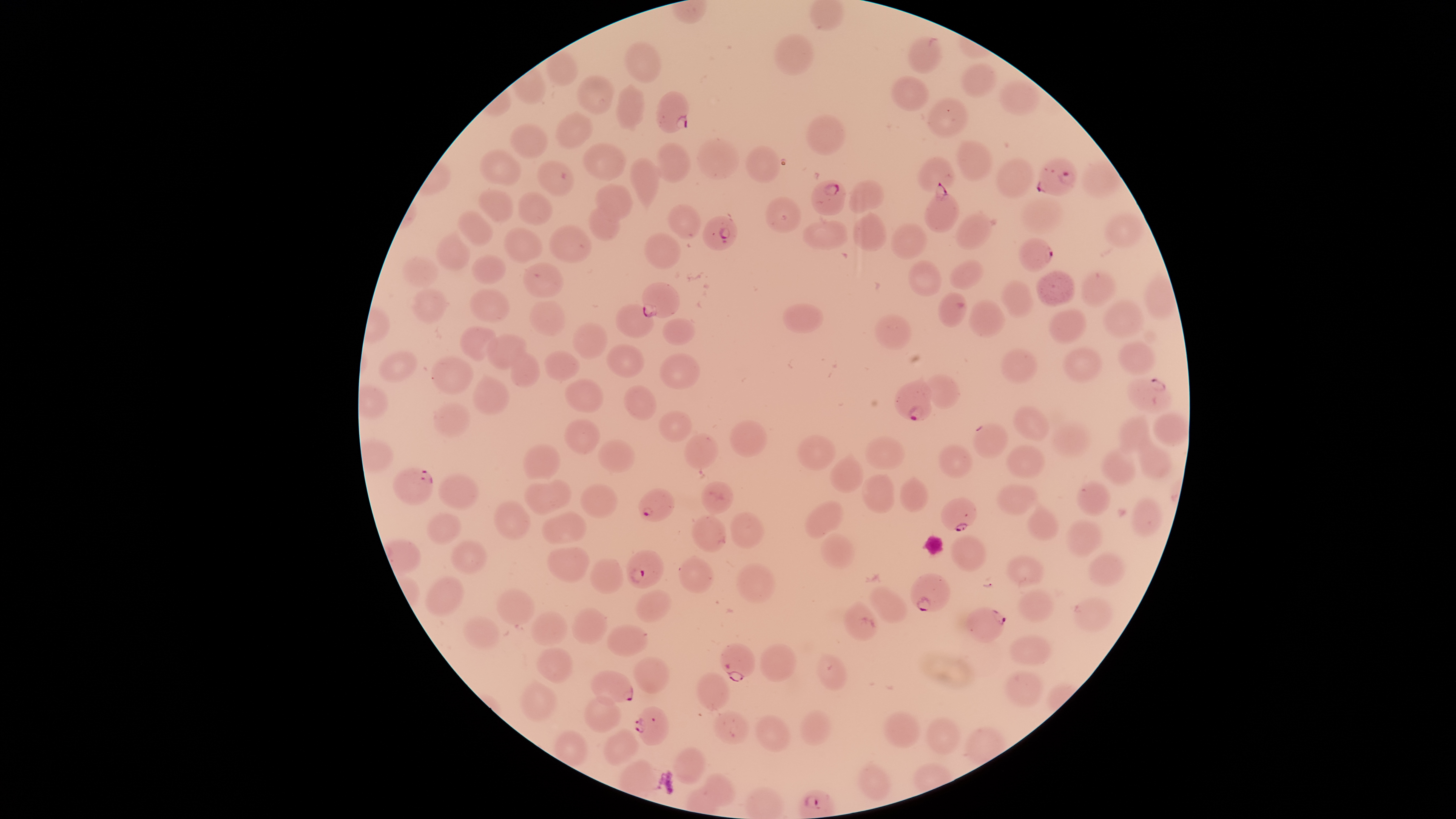
Approximate bounding boxes as [left, top, right, bottom] in pixels.
Summary:
  - Parasitized RBCs: [655, 90, 690, 134], [1036, 156, 1078, 196], [810, 180, 847, 216], [923, 182, 960, 232], [701, 214, 738, 251], [1017, 236, 1054, 273], [642, 282, 680, 318], [894, 374, 933, 421], [1125, 376, 1172, 413], [392, 466, 435, 506], [637, 486, 675, 522], [940, 497, 978, 532], [626, 549, 665, 589], [910, 572, 951, 613], [964, 607, 1007, 643], [719, 642, 756, 682], [590, 670, 633, 706], [633, 705, 670, 746]
  - Uninfected RBCs: [773, 33, 816, 75], [907, 34, 941, 73], [624, 39, 662, 84], [546, 50, 579, 87], [960, 63, 997, 97], [576, 73, 615, 115], [890, 75, 930, 111], [999, 78, 1040, 116], [616, 82, 646, 132], [926, 97, 969, 137], [555, 111, 594, 150], [806, 113, 847, 156], [509, 122, 550, 159], [696, 137, 740, 181], [954, 139, 993, 182], [581, 141, 627, 181], [653, 142, 692, 184], [745, 144, 780, 184], [479, 148, 522, 185], [995, 155, 1036, 198], [628, 156, 663, 213], [917, 156, 955, 191], [537, 159, 575, 197], [1081, 159, 1122, 199], [848, 179, 884, 214], [594, 183, 633, 222], [476, 188, 514, 223], [518, 190, 554, 226], [765, 195, 801, 234], [1021, 197, 1063, 232], [668, 204, 702, 240], [589, 207, 620, 242], [456, 209, 494, 247], [852, 211, 888, 252], [955, 211, 995, 249], [1103, 212, 1147, 249], [802, 220, 849, 249], [890, 222, 929, 260], [548, 223, 593, 264], [503, 226, 544, 264], [434, 228, 471, 271], [643, 232, 681, 271], [471, 254, 507, 285], [402, 256, 438, 288], [948, 259, 985, 291], [907, 260, 942, 296], [522, 261, 564, 298], [1035, 269, 1076, 307], [1081, 269, 1118, 307], [1000, 278, 1035, 319], [410, 286, 450, 325], [468, 288, 510, 322], [937, 292, 968, 328], [968, 298, 1006, 338], [1101, 298, 1146, 340], [528, 300, 567, 336], [615, 303, 655, 339], [781, 303, 824, 334], [1048, 307, 1087, 345], [874, 313, 912, 350], [662, 317, 697, 345], [572, 321, 609, 359], [459, 325, 497, 361], [486, 333, 528, 370], [1117, 340, 1156, 376], [605, 344, 645, 378], [1000, 347, 1039, 384], [1063, 347, 1104, 383], [377, 350, 417, 384], [509, 350, 541, 388], [543, 350, 581, 382], [659, 352, 700, 390], [430, 355, 475, 395], [921, 373, 961, 409], [472, 374, 510, 416], [564, 379, 604, 413], [624, 385, 658, 421], [433, 400, 471, 438], [1011, 405, 1051, 442], [657, 410, 692, 443], [1152, 413, 1188, 446], [1116, 414, 1150, 455], [563, 418, 601, 455], [729, 419, 769, 457], [972, 422, 1008, 459], [1050, 422, 1091, 458], [683, 431, 720, 471], [1137, 431, 1173, 481], [796, 434, 836, 471], [864, 434, 905, 470], [597, 439, 635, 473], [522, 443, 560, 479], [936, 444, 973, 478], [1005, 445, 1047, 480], [1099, 446, 1136, 486], [829, 450, 864, 493], [860, 472, 895, 514], [438, 473, 480, 512], [899, 475, 929, 513], [547, 479, 572, 508], [1074, 479, 1112, 516], [701, 480, 735, 515], [524, 483, 556, 516], [580, 483, 618, 519], [995, 484, 1038, 516], [1026, 497, 1060, 541], [1130, 497, 1162, 537], [803, 499, 844, 540], [493, 501, 532, 540], [541, 511, 588, 545], [729, 511, 765, 548], [426, 512, 462, 546], [691, 513, 726, 553], [1065, 518, 1105, 558], [820, 532, 856, 569], [949, 534, 987, 572], [449, 540, 488, 575], [546, 546, 590, 583], [1087, 552, 1126, 587], [1004, 553, 1046, 587], [678, 554, 715, 594], [589, 558, 624, 594], [735, 562, 776, 603], [424, 575, 465, 616], [869, 584, 909, 623], [495, 586, 535, 626], [1016, 588, 1055, 623], [636, 589, 673, 623], [1071, 596, 1114, 632], [842, 599, 881, 641], [571, 607, 608, 645], [531, 610, 568, 647], [462, 615, 500, 649], [606, 624, 648, 658], [1009, 634, 1054, 666], [759, 642, 797, 683], [535, 647, 573, 684], [816, 652, 847, 690], [632, 656, 670, 695], [1003, 670, 1045, 708], [696, 671, 730, 711], [519, 678, 558, 721], [584, 693, 622, 733], [799, 709, 832, 747], [713, 710, 750, 744], [882, 711, 922, 749], [754, 714, 791, 752], [925, 716, 962, 755], [602, 728, 640, 766], [552, 729, 589, 767], [672, 746, 706, 785], [855, 760, 892, 802], [699, 772, 737, 807]
  - Presence: malaria parasites detected
  - Capture: smartphone photograph through the microscope eyepiece
  - Stain: Giemsa
  - Preparation: thin blood film
  - Field of view: single
  - Species: Plasmodium falciparum
  - Visible region: circular
  - Image size: 1456×819 pixels